Give the extent of all Plasmodium malariae-infected red blood cells.
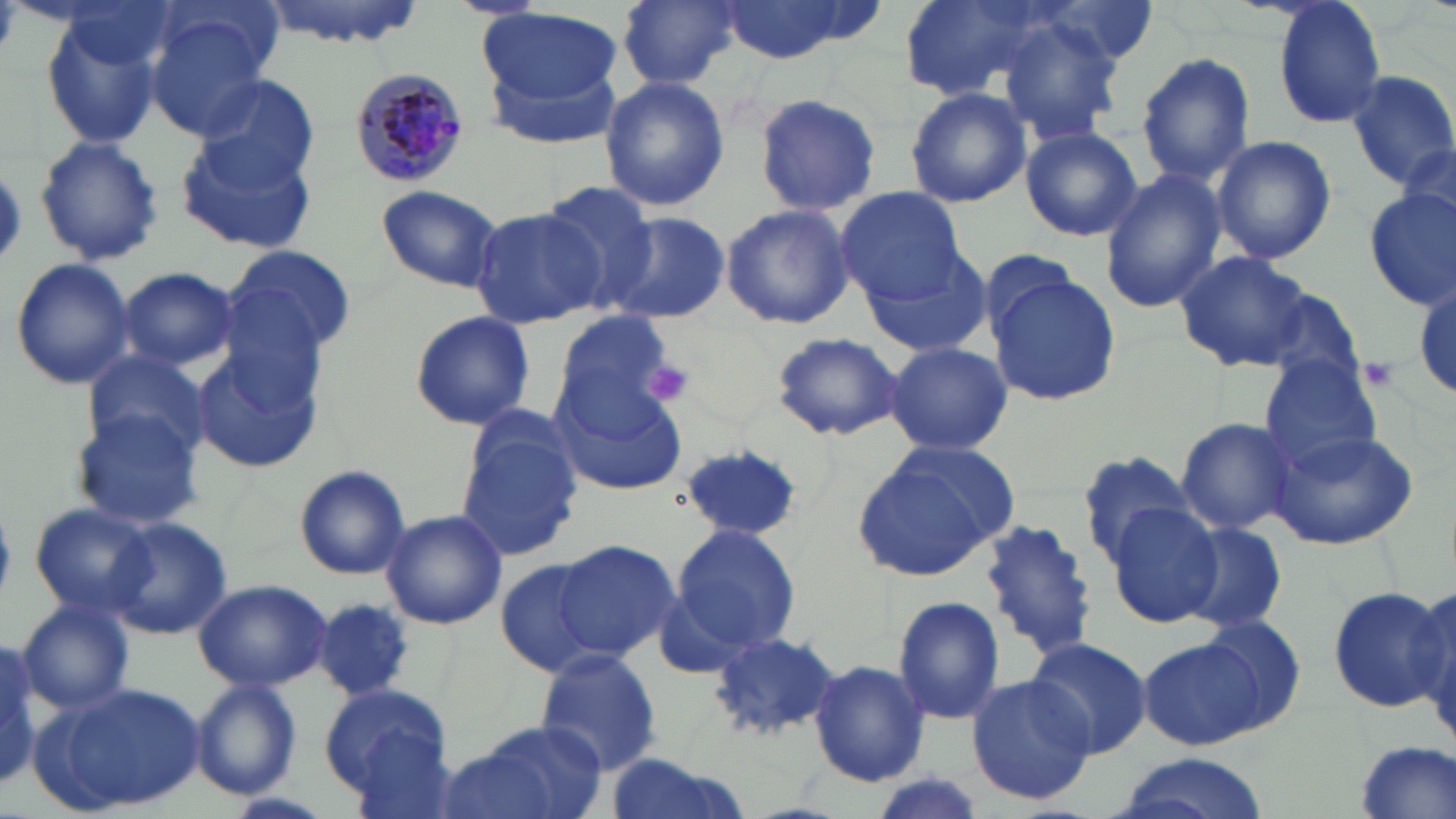

Approximate bounding boxes as named x1/y1/x2/y2 corners in pixels.
Plasmodium malariae-infected red blood cells: (x1=350, y1=68, x2=469, y2=186).

slide-level diagnosis = Plasmodium malariae
field of view = single
uninfected red blood cell locations = approximate bounding boxes as named x1/y1/x2/y2 corners in pixels: (x1=256, y1=0, x2=430, y2=49), (x1=619, y1=0, x2=741, y2=89), (x1=718, y1=0, x2=865, y2=64), (x1=903, y1=0, x2=1060, y2=102), (x1=1037, y1=0, x2=1157, y2=67), (x1=1272, y1=1, x2=1387, y2=130), (x1=481, y1=8, x2=624, y2=106), (x1=145, y1=11, x2=274, y2=140), (x1=42, y1=14, x2=160, y2=151), (x1=998, y1=17, x2=1122, y2=144), (x1=479, y1=44, x2=627, y2=149), (x1=1136, y1=53, x2=1255, y2=185), (x1=1346, y1=68, x2=1456, y2=190), (x1=195, y1=75, x2=322, y2=190), (x1=599, y1=77, x2=730, y2=213), (x1=904, y1=87, x2=1031, y2=208), (x1=754, y1=92, x2=882, y2=216), (x1=1020, y1=126, x2=1141, y2=241), (x1=177, y1=134, x2=316, y2=255), (x1=35, y1=135, x2=163, y2=267), (x1=1212, y1=135, x2=1335, y2=264), (x1=1099, y1=169, x2=1225, y2=313), (x1=539, y1=183, x2=659, y2=307), (x1=376, y1=184, x2=504, y2=292), (x1=1361, y1=187, x2=1455, y2=311), (x1=837, y1=189, x2=967, y2=304), (x1=721, y1=203, x2=853, y2=330), (x1=471, y1=206, x2=602, y2=330), (x1=603, y1=211, x2=730, y2=324), (x1=225, y1=245, x2=361, y2=361), (x1=1174, y1=250, x2=1313, y2=372), (x1=864, y1=251, x2=992, y2=358), (x1=9, y1=257, x2=136, y2=391), (x1=118, y1=267, x2=240, y2=371), (x1=986, y1=268, x2=1122, y2=407), (x1=1257, y1=288, x2=1366, y2=392), (x1=551, y1=307, x2=680, y2=425), (x1=407, y1=311, x2=538, y2=432), (x1=771, y1=331, x2=904, y2=441), (x1=882, y1=341, x2=1013, y2=457), (x1=191, y1=342, x2=324, y2=474), (x1=82, y1=349, x2=213, y2=461), (x1=1260, y1=356, x2=1384, y2=474), (x1=550, y1=382, x2=687, y2=496), (x1=71, y1=409, x2=202, y2=529), (x1=1174, y1=417, x2=1297, y2=535), (x1=1268, y1=426, x2=1421, y2=553), (x1=458, y1=433, x2=582, y2=559), (x1=675, y1=442, x2=807, y2=541), (x1=850, y1=443, x2=1019, y2=583), (x1=1078, y1=452, x2=1201, y2=566), (x1=296, y1=465, x2=410, y2=579), (x1=1106, y1=502, x2=1224, y2=626), (x1=28, y1=504, x2=156, y2=619), (x1=380, y1=510, x2=507, y2=631), (x1=106, y1=517, x2=233, y2=640), (x1=981, y1=520, x2=1097, y2=658), (x1=1174, y1=520, x2=1286, y2=635), (x1=670, y1=522, x2=801, y2=655), (x1=549, y1=539, x2=680, y2=662), (x1=498, y1=558, x2=610, y2=676), (x1=193, y1=579, x2=333, y2=692), (x1=1410, y1=584, x2=1456, y2=737), (x1=1327, y1=586, x2=1452, y2=712), (x1=892, y1=596, x2=1007, y2=724), (x1=17, y1=599, x2=135, y2=715), (x1=315, y1=600, x2=415, y2=699), (x1=1193, y1=616, x2=1307, y2=732), (x1=708, y1=630, x2=843, y2=742), (x1=0, y1=634, x2=48, y2=794), (x1=1023, y1=635, x2=1154, y2=758), (x1=1139, y1=639, x2=1262, y2=750), (x1=535, y1=648, x2=663, y2=778), (x1=808, y1=659, x2=931, y2=788), (x1=966, y1=674, x2=1096, y2=805), (x1=190, y1=679, x2=301, y2=801), (x1=40, y1=681, x2=209, y2=817), (x1=325, y1=685, x2=455, y2=807), (x1=447, y1=721, x2=609, y2=819), (x1=1348, y1=743, x2=1454, y2=819), (x1=598, y1=754, x2=752, y2=819), (x1=1109, y1=756, x2=1273, y2=819)
stain = May-Grünwald-Giemsa
magnification = 1000x
platelet locations = approximate bounding boxes as named x1/y1/x2/y2 corners in pixels: (x1=1358, y1=357, x2=1398, y2=391), (x1=641, y1=358, x2=697, y2=407)
modality = optical microscopy
preparation = thin blood smear
image size = 1456×819 pixels